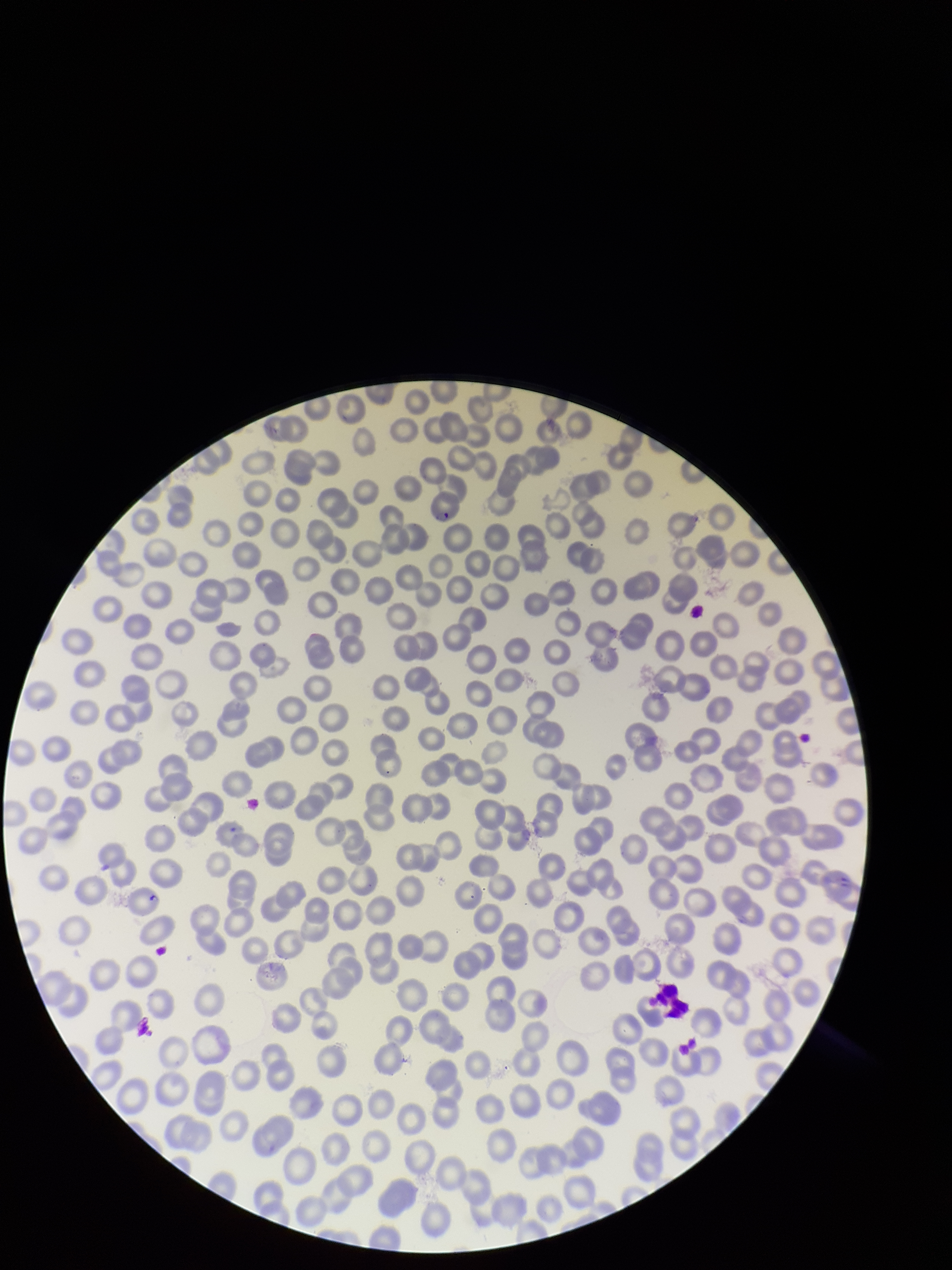
Summary:
  - Image size: 952×1270 pixels
  - Field of view: single
  - Parasitized red blood cell count: 1
  - Species reported for this patient: Plasmodium falciparum
  - Capture: smartphone photograph through the microscope eyepiece
  - Red blood cell count: 252
  - Stain: Giemsa
  - Parasitized red blood cells: identified
  - Patient malaria status: infected
  - Preparation: thin blood smear